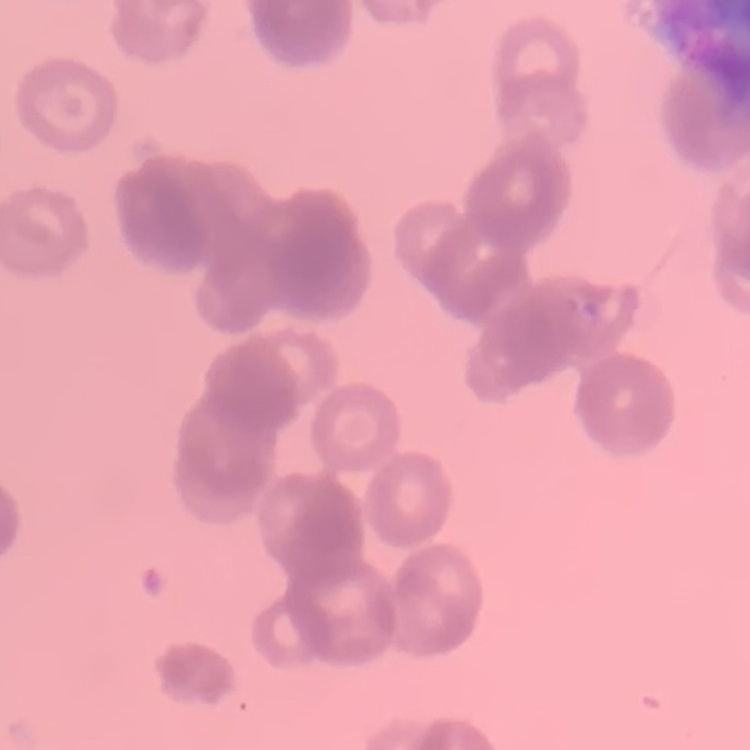

The red blood cells exhibit rouleaux formation. Square crop of a larger photomicrograph. Thin peripheral smear. Stained with either Field's or Giemsa.